Classify this cell by malaria status.
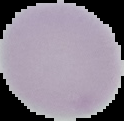

It is uninfected.

Summary:
  - Preparation: thin blood smear
  - Image type: segmented cell region on a black background
  - Image size: 124×121 pixels